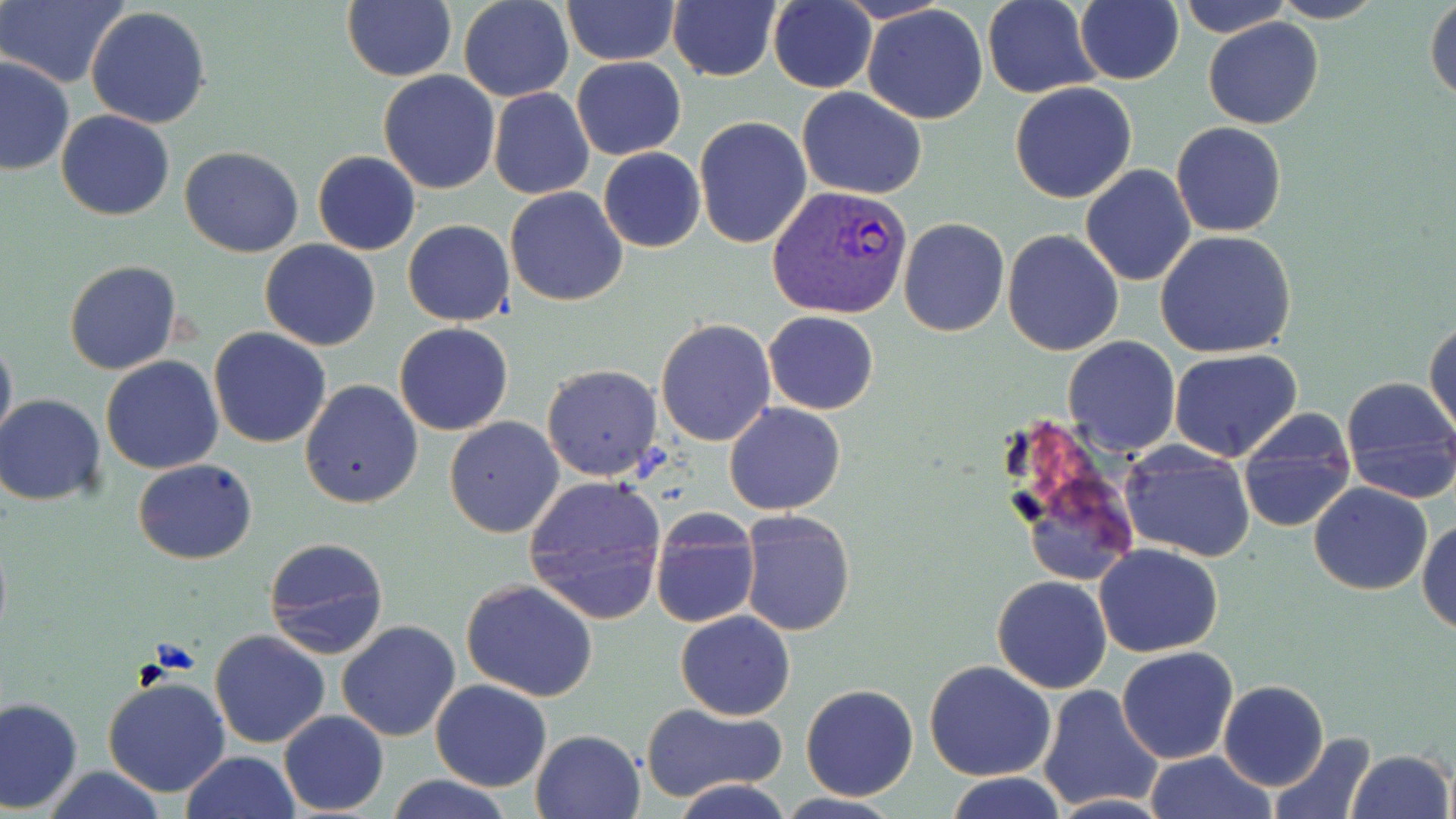
Approximate bounding boxes as named x1/y1/x2/y2 corners in pixels. Plasmodium vivax-infected red blood cell locations: (x1=765, y1=184, x2=914, y2=319). Uninfected red blood cell locations: (x1=1, y1=0, x2=126, y2=88), (x1=341, y1=0, x2=455, y2=83), (x1=458, y1=0, x2=575, y2=101), (x1=562, y1=0, x2=679, y2=65), (x1=666, y1=0, x2=781, y2=84), (x1=983, y1=0, x2=1104, y2=97), (x1=1076, y1=0, x2=1185, y2=85), (x1=1176, y1=0, x2=1295, y2=38), (x1=1268, y1=0, x2=1386, y2=23), (x1=768, y1=1, x2=876, y2=93), (x1=1425, y1=1, x2=1456, y2=103), (x1=85, y1=5, x2=212, y2=130), (x1=863, y1=5, x2=989, y2=125), (x1=1202, y1=15, x2=1324, y2=130), (x1=1, y1=55, x2=74, y2=175), (x1=571, y1=56, x2=685, y2=159), (x1=377, y1=71, x2=502, y2=195), (x1=1009, y1=82, x2=1138, y2=204), (x1=489, y1=86, x2=594, y2=200), (x1=797, y1=87, x2=928, y2=200), (x1=55, y1=110, x2=175, y2=221), (x1=693, y1=115, x2=812, y2=249), (x1=1171, y1=121, x2=1287, y2=237), (x1=179, y1=145, x2=305, y2=257), (x1=598, y1=148, x2=705, y2=253), (x1=313, y1=152, x2=420, y2=255), (x1=1079, y1=164, x2=1197, y2=285), (x1=505, y1=186, x2=629, y2=307), (x1=898, y1=218, x2=1009, y2=337), (x1=402, y1=220, x2=515, y2=326), (x1=1002, y1=230, x2=1124, y2=355), (x1=1156, y1=230, x2=1298, y2=358), (x1=260, y1=239, x2=380, y2=351), (x1=64, y1=261, x2=182, y2=375), (x1=762, y1=311, x2=880, y2=415), (x1=654, y1=317, x2=778, y2=447), (x1=1426, y1=318, x2=1456, y2=442), (x1=394, y1=322, x2=515, y2=436), (x1=208, y1=328, x2=331, y2=448), (x1=0, y1=329, x2=16, y2=451), (x1=1063, y1=336, x2=1182, y2=457), (x1=1169, y1=348, x2=1301, y2=463), (x1=100, y1=356, x2=225, y2=474), (x1=540, y1=364, x2=664, y2=482), (x1=1337, y1=375, x2=1456, y2=504), (x1=298, y1=379, x2=422, y2=509), (x1=0, y1=394, x2=107, y2=506), (x1=724, y1=403, x2=846, y2=515), (x1=1235, y1=410, x2=1358, y2=535), (x1=444, y1=416, x2=564, y2=538), (x1=1004, y1=443, x2=1144, y2=595), (x1=1119, y1=447, x2=1256, y2=564), (x1=132, y1=458, x2=257, y2=564), (x1=522, y1=474, x2=668, y2=622), (x1=1308, y1=482, x2=1434, y2=596), (x1=738, y1=512, x2=854, y2=637), (x1=649, y1=514, x2=760, y2=629), (x1=1417, y1=518, x2=1456, y2=635), (x1=261, y1=534, x2=389, y2=661), (x1=1093, y1=544, x2=1224, y2=657), (x1=991, y1=575, x2=1111, y2=693), (x1=462, y1=579, x2=600, y2=702), (x1=675, y1=610, x2=797, y2=720), (x1=336, y1=620, x2=461, y2=742), (x1=210, y1=630, x2=329, y2=749), (x1=1116, y1=646, x2=1239, y2=765), (x1=924, y1=661, x2=1056, y2=782), (x1=102, y1=676, x2=232, y2=799), (x1=429, y1=679, x2=552, y2=792), (x1=1217, y1=680, x2=1329, y2=791), (x1=800, y1=684, x2=918, y2=800), (x1=1037, y1=686, x2=1163, y2=813), (x1=0, y1=696, x2=83, y2=813), (x1=640, y1=703, x2=787, y2=802), (x1=278, y1=711, x2=388, y2=815), (x1=531, y1=729, x2=645, y2=819), (x1=1268, y1=731, x2=1378, y2=818), (x1=1344, y1=749, x2=1453, y2=819), (x1=181, y1=750, x2=300, y2=819), (x1=1145, y1=750, x2=1275, y2=819), (x1=39, y1=767, x2=168, y2=819), (x1=948, y1=773, x2=1065, y2=819), (x1=385, y1=774, x2=513, y2=819), (x1=669, y1=777, x2=793, y2=819), (x1=774, y1=793, x2=905, y2=819), (x1=1045, y1=794, x2=1173, y2=819). Slide-level diagnosis: Plasmodium vivax. One field of a larger specimen. Image is 1456×819 pixels. Optical microscopy. Thin blood smear. Captured at 1000x magnification. May-Grünwald-Giemsa-stained preparation.